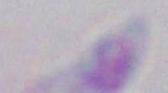
Micrograph. 1000x magnification. Toxoplasma gondii is shown.